Name the cell type shown.
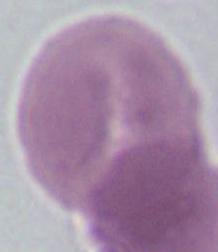
An erythrocyte.

{
  "modality": "micrograph",
  "magnification": "1000x"
}